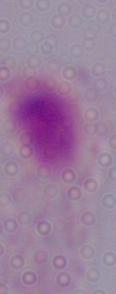
Micrograph. A trichomonad is shown. 1000x magnification.